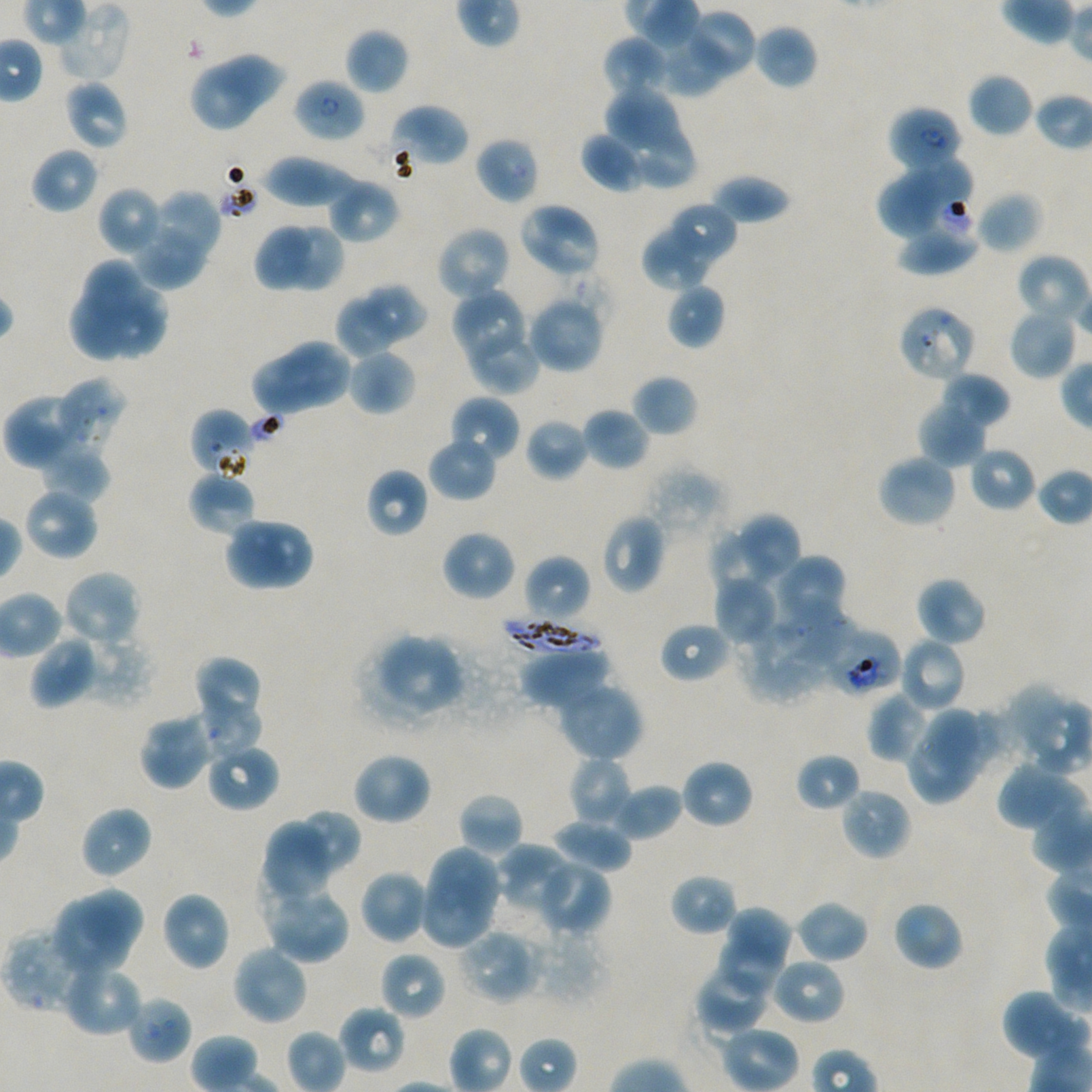
Not every red blood cell is marked. A life-cycle stage — or a range of stages, where the recorded stages span more than one — follows each staged infected red blood cell.
field of view = single
locations of red blood cells of indeterminate infection status = approximate bounding boxes as [x1, y1, x2, y2] in pixels: [897, 304, 978, 383], [189, 408, 257, 479], [817, 626, 902, 698]
locations of uninfected red blood cells = approximate bounding boxes as [x1, y1, x2, y2] in pixels: [56, 1, 131, 80], [691, 9, 757, 74], [752, 23, 818, 90], [344, 28, 409, 94], [602, 36, 670, 101], [661, 43, 733, 96], [217, 54, 286, 114], [189, 65, 255, 133], [968, 71, 1035, 137], [63, 79, 129, 151], [604, 86, 686, 160], [390, 104, 469, 167], [579, 132, 647, 194], [627, 132, 695, 187], [475, 137, 539, 204], [30, 147, 99, 215], [913, 153, 972, 216], [262, 155, 364, 207], [879, 168, 941, 238], [711, 172, 792, 225], [327, 179, 399, 243], [97, 185, 164, 256], [149, 189, 222, 265], [976, 192, 1042, 254], [519, 201, 602, 280], [666, 202, 736, 268], [897, 219, 979, 276], [253, 221, 311, 291], [253, 221, 345, 294], [132, 222, 204, 289], [293, 223, 344, 290], [435, 225, 511, 302], [642, 225, 714, 289], [1014, 253, 1090, 329], [86, 257, 142, 325], [666, 283, 725, 350], [362, 285, 428, 344], [106, 287, 169, 359], [450, 288, 529, 365], [69, 291, 126, 363], [526, 294, 605, 374], [335, 298, 397, 357], [1008, 305, 1079, 381], [465, 323, 541, 394], [280, 337, 352, 412], [346, 348, 416, 416], [250, 359, 323, 416], [941, 371, 1011, 429], [632, 374, 698, 437], [55, 377, 126, 450], [5, 390, 90, 469], [448, 395, 521, 465], [918, 400, 987, 468], [581, 407, 651, 471], [525, 418, 589, 481], [427, 435, 497, 502], [41, 444, 111, 503], [969, 446, 1036, 511], [875, 454, 958, 529], [365, 468, 429, 539], [187, 471, 256, 536], [22, 487, 99, 562], [736, 512, 802, 583], [601, 513, 666, 594], [223, 518, 286, 592], [259, 518, 315, 592], [440, 529, 516, 602], [707, 532, 774, 600], [524, 554, 592, 625], [778, 554, 848, 624], [61, 569, 143, 648], [714, 574, 778, 647], [915, 577, 987, 647], [776, 608, 851, 668], [659, 622, 731, 683], [505, 626, 608, 687], [83, 633, 153, 707], [380, 633, 465, 706], [29, 634, 98, 710], [898, 636, 967, 712], [517, 645, 610, 708], [193, 655, 266, 719], [556, 681, 644, 763], [1000, 685, 1069, 755], [867, 690, 929, 763], [198, 700, 263, 761], [922, 707, 983, 777], [138, 712, 216, 790], [205, 740, 279, 813], [906, 740, 975, 803], [351, 751, 432, 826], [795, 752, 861, 813], [569, 756, 633, 828], [680, 759, 754, 829], [998, 762, 1063, 826], [613, 782, 684, 841], [839, 786, 911, 862], [458, 792, 524, 858], [79, 805, 153, 879], [298, 808, 360, 871], [261, 818, 337, 905], [551, 819, 632, 875], [496, 843, 575, 913], [428, 844, 503, 913], [534, 858, 611, 936], [359, 869, 429, 945], [670, 873, 738, 936], [418, 876, 494, 950], [261, 884, 350, 963], [78, 888, 143, 956], [160, 890, 231, 972], [52, 899, 122, 976], [793, 899, 869, 965], [892, 900, 964, 971], [730, 907, 790, 972], [3, 928, 94, 1013], [457, 928, 541, 1004], [717, 943, 782, 996], [231, 944, 309, 1027], [379, 951, 445, 1021], [770, 956, 846, 1025], [695, 960, 774, 1034], [61, 962, 144, 1038], [1002, 990, 1087, 1063], [126, 994, 192, 1064], [338, 1004, 407, 1074]
stain = Giemsa
objective = 100x, oil immersion, numerical aperture 1.45
culture = in-vitro Plasmodium falciparum strain NF54, static
preparation = thin blood film
donor blood group = A+/O+
image size = 1092×1092 pixels
locations of infected red blood cells = approximate bounding boxes as [x1, y1, x2, y2] in pixels: [293, 77, 366, 143] ring; [887, 105, 963, 174] early ring to early trophozoite; [498, 615, 600, 659]